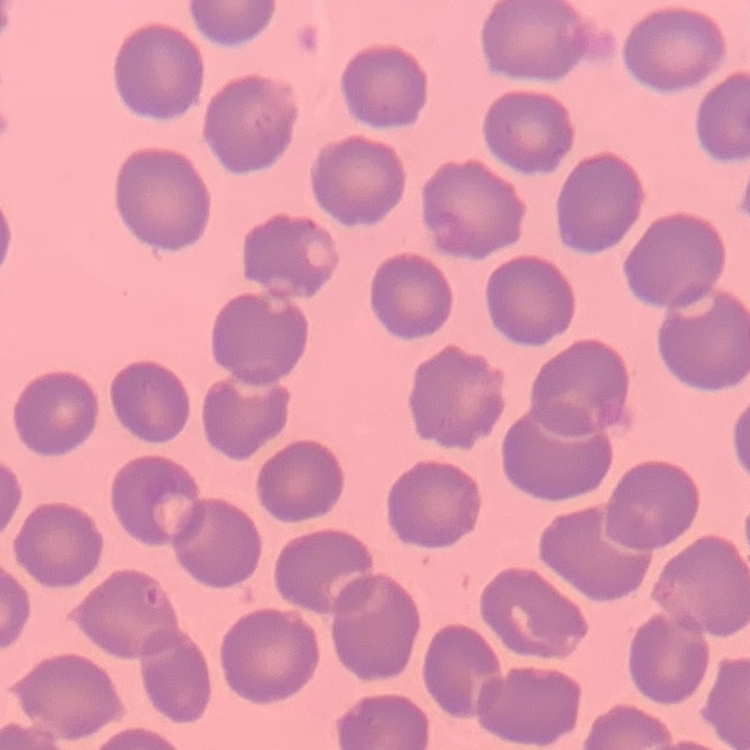 The red blood cells exhibit no rouleaux formation. Thin peripheral smear. Stained with either Field's or Giemsa. One tile cut from a larger photomicrograph.